Identify the parasite.
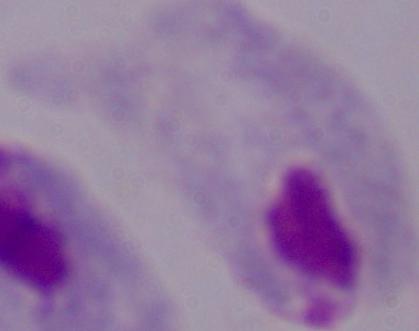

This is a trichomonad.

1000x magnification. Photomicrograph.